Locate every blood parasite and identify its species.
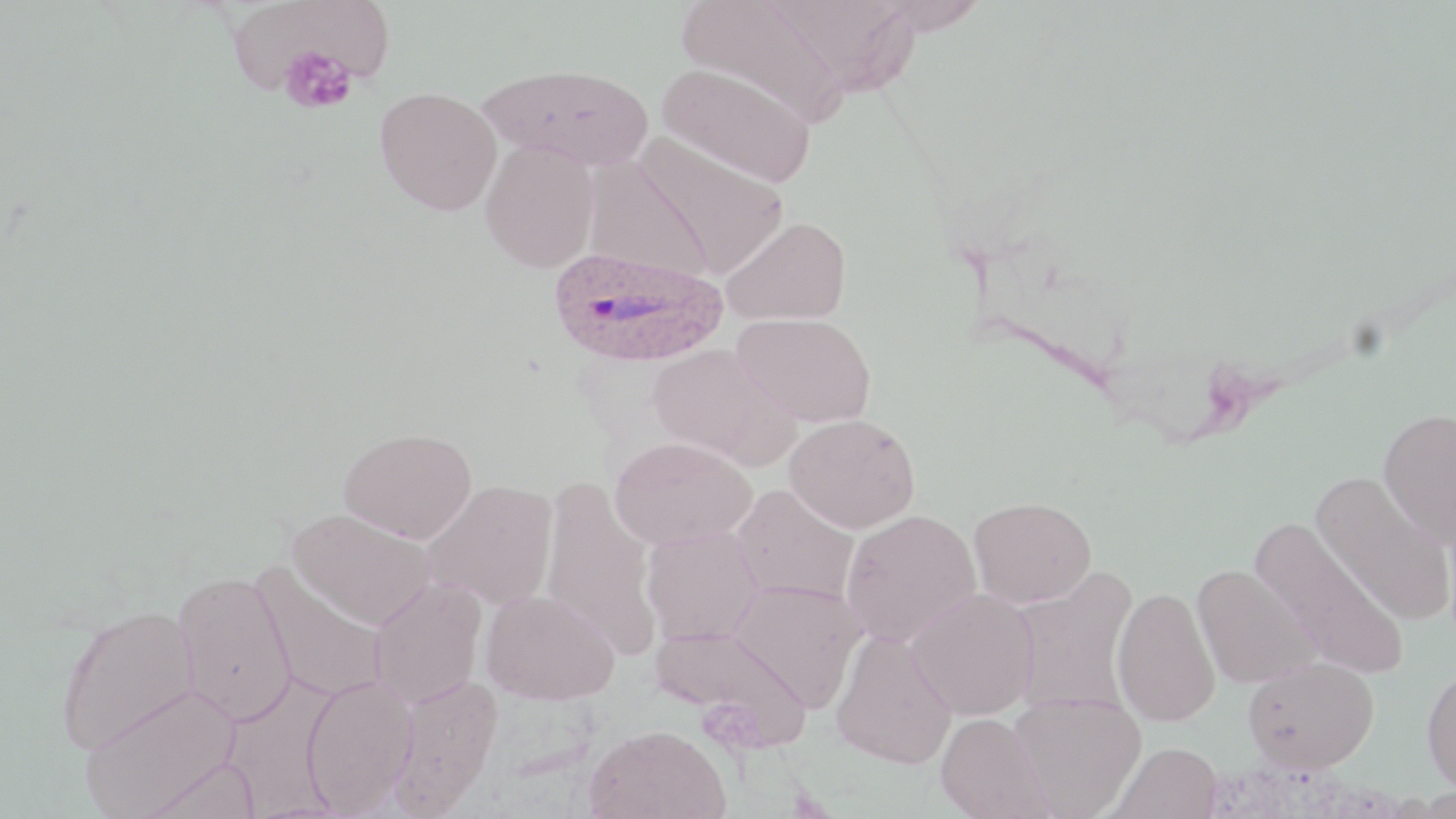

Approximate bounding boxes as named x1/y1/x2/y2 corners in pixels.
Plasmodium ovale-infected red blood cells: (x1=547, y1=246, x2=728, y2=368).
No Plasmodium falciparum, Plasmodium malariae, Plasmodium vivax, Babesia divergens, or Trypanosoma brucei observed.

Platelet locations: (x1=278, y1=45, x2=359, y2=114). Uninfected red blood cell locations: (x1=677, y1=0, x2=847, y2=129), (x1=868, y1=0, x2=991, y2=35), (x1=766, y1=1, x2=922, y2=96), (x1=235, y1=5, x2=395, y2=91), (x1=480, y1=63, x2=654, y2=171), (x1=657, y1=63, x2=816, y2=188), (x1=374, y1=86, x2=502, y2=215), (x1=632, y1=133, x2=790, y2=277), (x1=480, y1=140, x2=599, y2=273), (x1=582, y1=157, x2=714, y2=281), (x1=720, y1=215, x2=853, y2=327), (x1=732, y1=313, x2=877, y2=427), (x1=646, y1=342, x2=797, y2=469), (x1=1377, y1=407, x2=1456, y2=547), (x1=784, y1=413, x2=920, y2=533), (x1=338, y1=426, x2=478, y2=543), (x1=609, y1=435, x2=757, y2=549), (x1=1310, y1=471, x2=1454, y2=627), (x1=538, y1=476, x2=663, y2=659), (x1=422, y1=479, x2=558, y2=611), (x1=731, y1=484, x2=860, y2=607), (x1=968, y1=497, x2=1097, y2=607), (x1=288, y1=508, x2=437, y2=630), (x1=840, y1=508, x2=982, y2=648), (x1=1251, y1=519, x2=1409, y2=682), (x1=641, y1=526, x2=764, y2=644), (x1=251, y1=563, x2=389, y2=704), (x1=1191, y1=564, x2=1321, y2=688), (x1=1007, y1=566, x2=1140, y2=715), (x1=173, y1=569, x2=297, y2=726), (x1=368, y1=577, x2=487, y2=709), (x1=729, y1=579, x2=867, y2=711), (x1=1111, y1=585, x2=1221, y2=727), (x1=907, y1=587, x2=1040, y2=720), (x1=481, y1=588, x2=620, y2=704), (x1=56, y1=604, x2=199, y2=754), (x1=652, y1=623, x2=810, y2=748), (x1=831, y1=629, x2=958, y2=769), (x1=1242, y1=656, x2=1379, y2=773), (x1=1421, y1=665, x2=1456, y2=795), (x1=302, y1=674, x2=418, y2=816), (x1=386, y1=675, x2=504, y2=816), (x1=79, y1=684, x2=242, y2=818), (x1=1008, y1=693, x2=1145, y2=818), (x1=936, y1=712, x2=1051, y2=819), (x1=585, y1=723, x2=730, y2=819), (x1=1110, y1=742, x2=1223, y2=819), (x1=142, y1=757, x2=262, y2=819). Slide-level diagnosis: Plasmodium ovale. Image is 1456×819 pixels. Captured at 1000x magnification. May-Grünwald-Giemsa-stained preparation. Light microscopy. Thin blood smear. Single field of view.